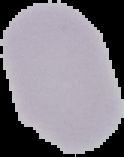
{
  "preparation": "thin blood film",
  "image_type": "segmented cell region on a black background",
  "result": "negative for malaria parasites",
  "image_size": "124×157 pixels"
}